Locate every Plasmodium parasite.
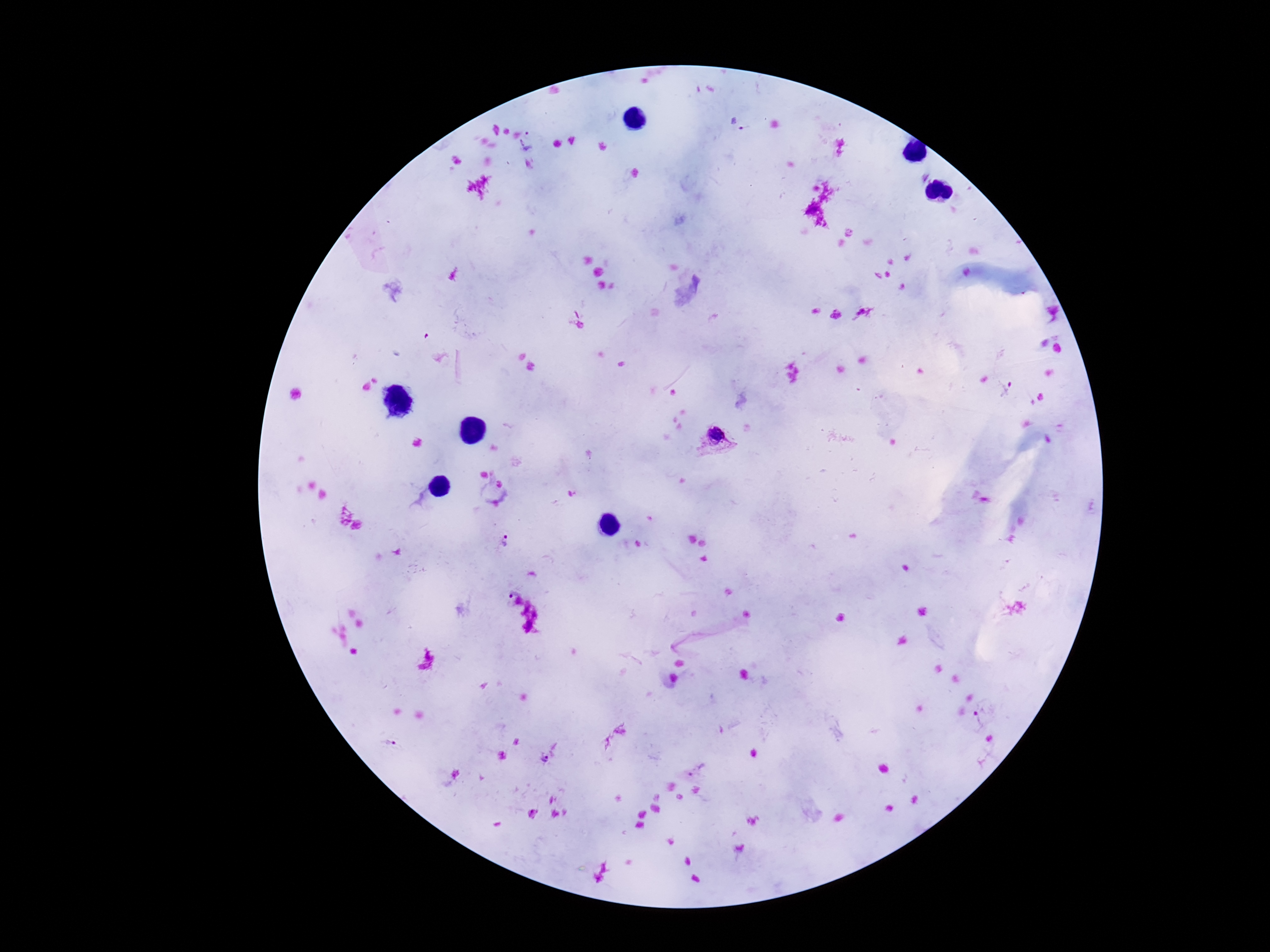

Approximate object centers, in pixels from the top-left corner.
Plasmodium parasites: (x=745, y=129), (x=528, y=141), (x=1007, y=388), (x=718, y=440), (x=505, y=542), (x=512, y=592), (x=979, y=720), (x=388, y=743), (x=543, y=760), (x=699, y=769).

{
  "preparation": "thick blood smear",
  "patient_malaria_status": "positive",
  "image_size": "1270×952 pixels",
  "stain": "Giemsa",
  "field_of_view": "single",
  "capture": "smartphone camera through the microscope eyepiece",
  "magnification": "100x"
}